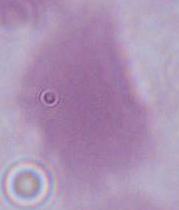

1000x magnification. A red blood cell is seen. Photomicrograph.